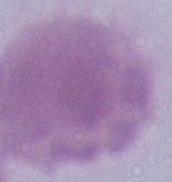
1000x magnification. Photomicrograph. A red blood cell is seen.